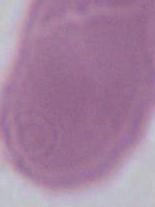
Summary:
  - Magnification: 1000x
  - Modality: micrograph
  - Identification: erythrocyte